Classify this cell by malaria status.
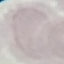
Uninfected.

stain: Giemsa
image_type: cell patch, automatically extracted from a larger field of view and resized to 64 × 64 pixels
preparation: thin blood smear
capture: smartphone through the microscope eyepiece